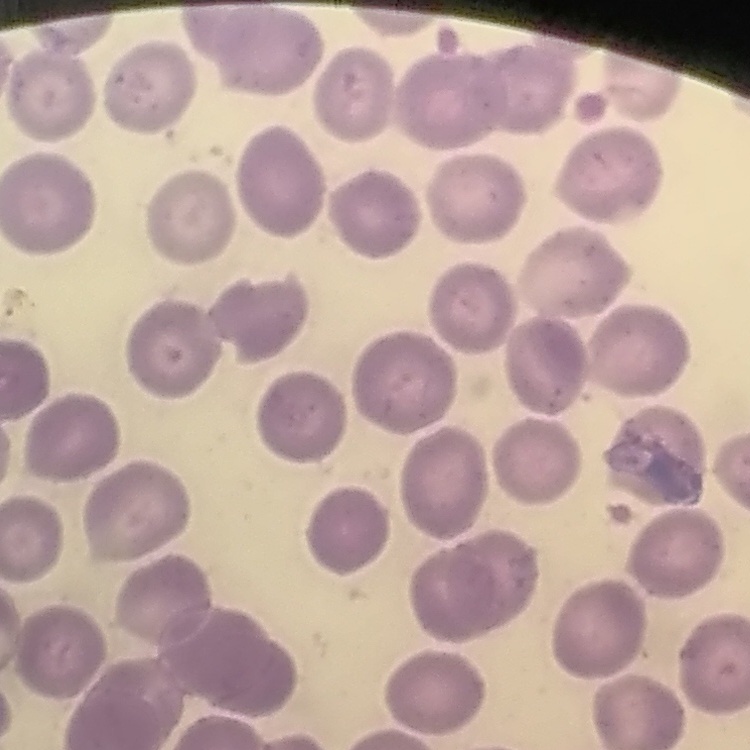
{
  "red_blood_cell_morphology": "no rouleaux formation",
  "stain": "Field's or Giemsa",
  "image_type": "square crop of a larger photomicrograph",
  "preparation": "thin peripheral smear"
}